Classify this cell by malaria status.
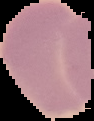
Uninfected.

The area outside the segmented cell region is set to black. Image is 94×121 pixels. From a thin blood film.